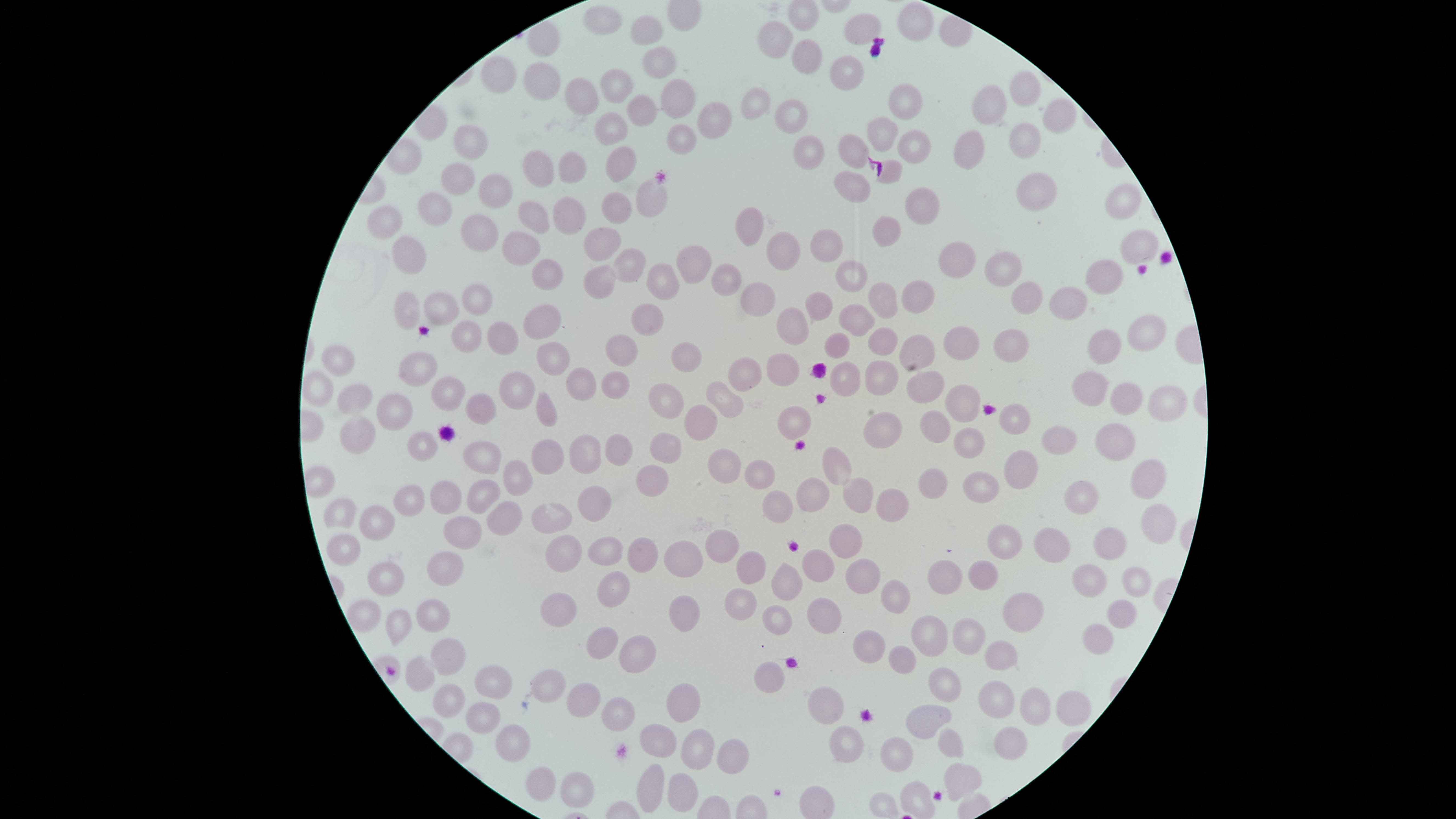

Approximate bounding boxes as [left, top, right, bottom] in pixels.
Summary:
  - Uninfected red blood cells: [899, 2, 934, 41], [584, 6, 621, 36], [843, 13, 882, 46], [631, 16, 663, 45], [756, 21, 793, 60], [792, 39, 823, 73], [643, 46, 677, 78], [482, 55, 517, 96], [829, 56, 867, 92], [523, 62, 560, 101], [600, 68, 635, 103], [1009, 69, 1039, 107], [564, 78, 599, 118], [661, 78, 696, 119], [889, 84, 924, 120], [972, 85, 1010, 125], [738, 87, 768, 120], [627, 95, 658, 126], [773, 99, 808, 134], [1044, 99, 1079, 131], [698, 101, 731, 138], [595, 111, 627, 145], [867, 116, 900, 153], [1007, 122, 1041, 160], [453, 124, 490, 162], [666, 124, 699, 156], [897, 129, 930, 164], [953, 130, 986, 171], [839, 134, 870, 168], [792, 135, 826, 172], [606, 145, 636, 183], [521, 150, 556, 187], [561, 151, 587, 183], [878, 159, 903, 185], [442, 164, 477, 197], [1015, 170, 1058, 212], [833, 172, 872, 204], [479, 174, 515, 211], [636, 177, 669, 218], [1107, 182, 1140, 219], [904, 187, 941, 224], [602, 191, 632, 224], [417, 192, 452, 228], [554, 196, 586, 235], [517, 201, 551, 236], [368, 205, 403, 240], [734, 206, 764, 246], [462, 214, 498, 251], [873, 215, 901, 247], [584, 226, 622, 264], [813, 228, 844, 263], [504, 231, 540, 266], [1122, 231, 1158, 266], [767, 232, 801, 272], [392, 235, 427, 276], [678, 244, 711, 284], [937, 244, 975, 278], [612, 247, 645, 283], [985, 250, 1024, 288], [532, 258, 563, 289], [837, 259, 868, 292], [1086, 259, 1122, 296], [713, 262, 741, 296], [647, 263, 681, 301], [584, 267, 616, 301], [902, 279, 936, 316], [1012, 281, 1042, 314], [742, 282, 777, 317], [869, 282, 899, 321], [461, 284, 493, 314], [1050, 287, 1087, 320], [423, 289, 461, 327], [392, 291, 420, 329], [806, 292, 834, 321], [524, 303, 561, 339], [631, 303, 664, 336], [838, 303, 874, 338], [776, 307, 810, 345], [1126, 316, 1166, 352], [452, 321, 482, 352], [488, 322, 518, 355], [868, 327, 897, 356], [944, 327, 981, 362], [993, 327, 1029, 365], [1087, 329, 1122, 364], [825, 332, 850, 359], [605, 334, 638, 365], [900, 335, 934, 370], [536, 341, 570, 376], [671, 342, 701, 373], [322, 345, 355, 377], [399, 351, 440, 386], [766, 353, 802, 386], [729, 358, 763, 393], [864, 359, 899, 396], [831, 362, 860, 397], [567, 367, 596, 402], [603, 371, 629, 400], [906, 371, 944, 404], [1071, 371, 1110, 407], [302, 372, 334, 406], [499, 372, 535, 409], [432, 377, 466, 410], [649, 382, 684, 420], [707, 383, 743, 417], [945, 383, 978, 424], [1111, 383, 1142, 415], [337, 384, 372, 414], [1148, 386, 1190, 420], [535, 391, 558, 426], [465, 392, 497, 424], [378, 394, 414, 430], [683, 404, 716, 441], [998, 404, 1030, 434], [777, 406, 813, 439], [863, 411, 903, 449], [919, 411, 951, 443], [339, 417, 375, 454], [1095, 424, 1137, 462], [1042, 425, 1076, 455], [953, 428, 986, 459], [408, 431, 438, 460], [651, 432, 681, 463], [570, 434, 601, 475], [606, 434, 633, 467], [533, 440, 564, 474], [463, 442, 503, 474], [821, 446, 853, 486], [709, 447, 741, 484], [1005, 449, 1038, 490], [1130, 458, 1167, 499], [504, 460, 534, 497], [745, 461, 777, 488], [635, 465, 670, 498], [920, 468, 947, 498], [963, 471, 998, 503], [795, 476, 831, 513], [843, 478, 874, 513], [466, 479, 501, 514], [431, 480, 460, 515], [1064, 480, 1097, 515], [392, 484, 425, 518], [577, 486, 612, 523], [877, 489, 910, 522], [762, 491, 794, 524], [325, 497, 357, 528], [486, 502, 522, 536], [530, 502, 573, 535], [1141, 503, 1176, 544], [359, 505, 396, 539], [444, 516, 483, 550], [831, 524, 861, 557], [988, 525, 1020, 560], [1034, 527, 1071, 563], [1094, 527, 1126, 561], [704, 529, 740, 563], [327, 534, 360, 565], [545, 535, 582, 571], [588, 536, 625, 564], [627, 537, 658, 573], [664, 540, 702, 577], [803, 549, 835, 582], [427, 551, 464, 586], [736, 551, 767, 584], [846, 558, 879, 593], [969, 560, 999, 589], [368, 561, 406, 595], [927, 561, 961, 596], [771, 563, 803, 600], [1071, 564, 1106, 597], [1122, 567, 1150, 597], [597, 571, 630, 608], [881, 579, 911, 614], [725, 588, 758, 620], [1002, 592, 1043, 633], [540, 593, 578, 627], [669, 594, 700, 632], [806, 597, 842, 633], [415, 599, 449, 631], [1108, 600, 1137, 629], [347, 601, 381, 633], [761, 604, 792, 634], [385, 608, 412, 647], [911, 615, 947, 654], [952, 618, 987, 655], [1082, 624, 1113, 655], [587, 626, 618, 660], [853, 630, 886, 664], [618, 635, 657, 673], [431, 638, 467, 675], [984, 641, 1017, 669], [888, 645, 918, 674], [405, 657, 436, 691], [753, 661, 785, 693], [474, 665, 512, 698], [929, 667, 961, 701], [531, 669, 566, 703], [977, 680, 1014, 719], [567, 683, 601, 718], [667, 683, 701, 724], [433, 684, 464, 719], [807, 686, 845, 724], [1020, 687, 1050, 726], [1057, 691, 1092, 726], [600, 695, 635, 731], [466, 702, 500, 734], [906, 704, 951, 738], [639, 723, 677, 759], [495, 724, 529, 762], [829, 725, 864, 765], [995, 726, 1027, 760], [682, 727, 714, 770], [938, 727, 965, 757], [881, 736, 914, 773], [718, 737, 750, 773], [636, 763, 664, 812], [943, 763, 981, 801], [526, 767, 557, 802], [559, 770, 593, 808], [667, 772, 698, 813], [900, 780, 934, 816]
  - Field of view: single
  - Preparation: thin blood smear
  - Visible region: circular
  - Presence: no malaria parasites detected
  - Image size: 1456×819 pixels
  - Stain: Giemsa
  - Capture: smartphone photograph through the microscope eyepiece